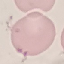
Result: negative for malaria parasites. Giemsa-stained preparation. Automatically extracted cell patch, resized to 64 × 64 pixels. Thin blood smear. Acquired by smartphone through the microscope eyepiece.